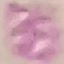
malaria_status: uninfected
preparation: thin blood film
stain: Giemsa
capture: smartphone through the microscope eyepiece
image_type: automatically extracted cell patch, resized to 64 × 64 pixels